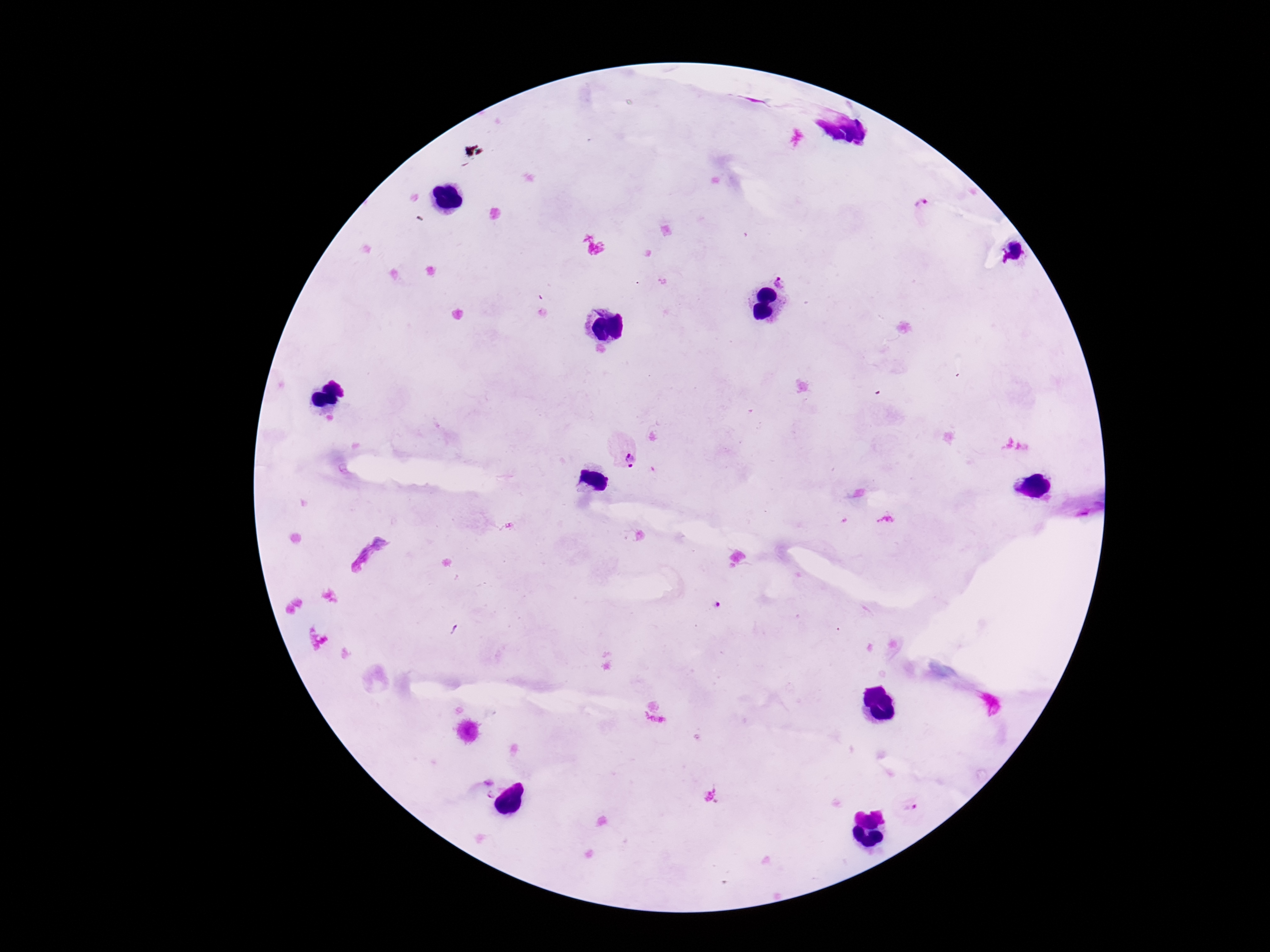

field of view = one from this slide
image size = 1270×952 pixels
capture = smartphone camera through the microscope eyepiece
preparation = thick blood film
Plasmodium parasite locations = approximate centers as (x, y) in pixels: (921, 206), (785, 279), (622, 446), (716, 605), (488, 781), (489, 796), (912, 810)
magnification = 100x
stain = Giemsa
patient malaria status = infected